Name the parasite shown.
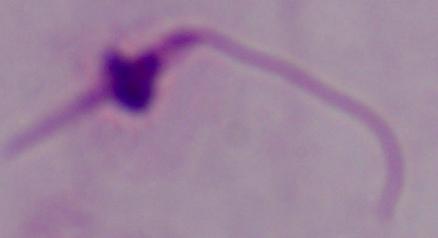
This is Leishmania.

Summary:
  - Modality: micrograph
  - Magnification: 1000x